Outline each blood parasite and name the species.
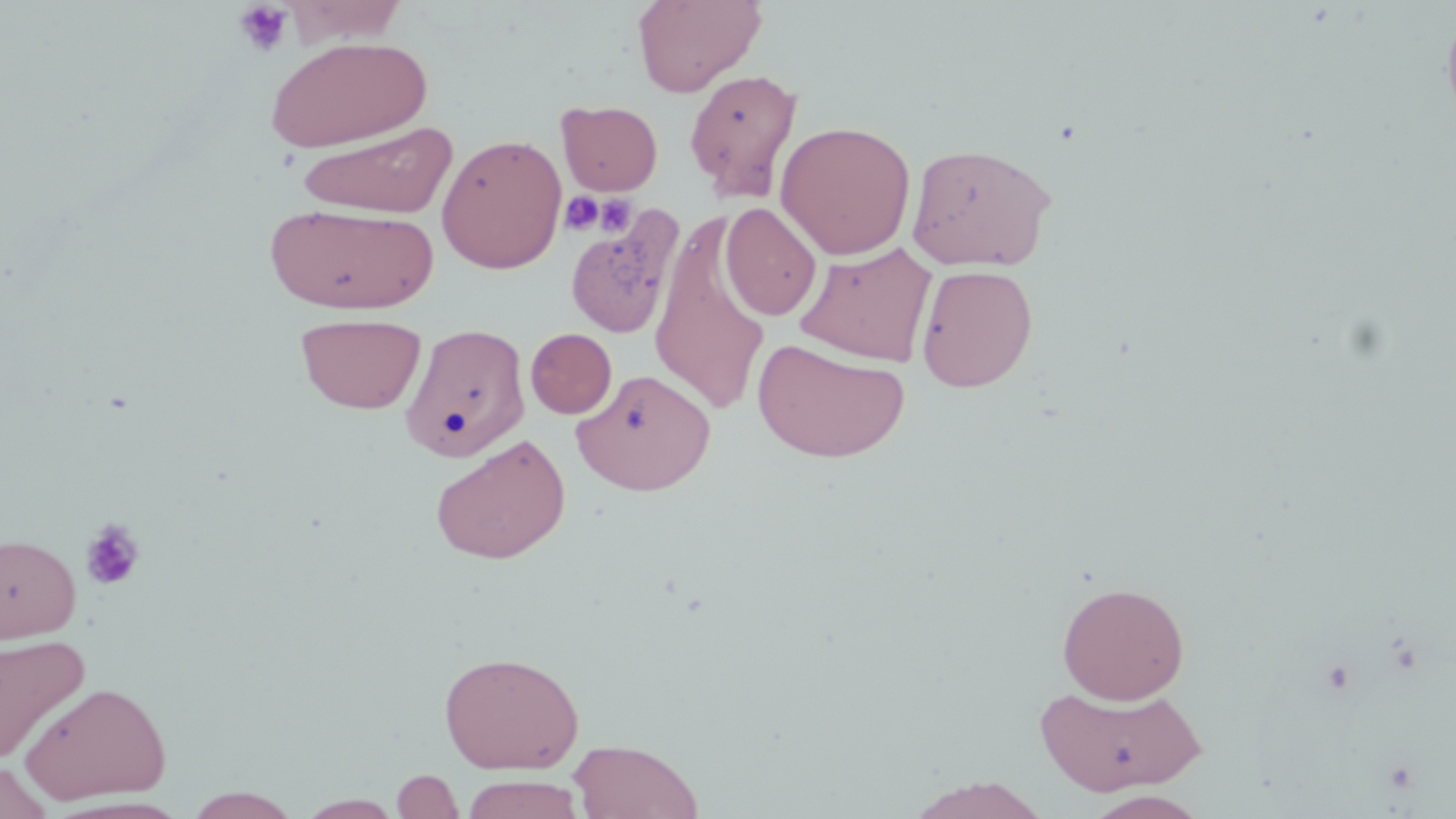

No blood parasites seen.

Summary:
  - Coordinate format: approximate bounding boxes as (x1, y1, x2, y2) in pixels
  - Uninfected red blood cell locations: (631, 0, 767, 97), (1441, 6, 1456, 131), (264, 35, 432, 153), (683, 68, 803, 201), (556, 99, 663, 195), (775, 120, 916, 260), (296, 122, 458, 219), (436, 133, 567, 274), (906, 142, 1057, 271), (265, 201, 438, 315), (720, 202, 822, 321), (564, 208, 683, 341), (649, 214, 773, 416), (794, 241, 937, 366), (915, 264, 1039, 392), (295, 313, 427, 414), (401, 322, 530, 463), (526, 328, 617, 418), (753, 337, 911, 463), (572, 369, 716, 495), (430, 434, 571, 564), (0, 533, 81, 643), (1056, 581, 1190, 704), (0, 633, 90, 764), (438, 650, 585, 774), (19, 681, 172, 805), (1036, 682, 1206, 796), (568, 739, 704, 819), (1, 758, 53, 818), (391, 769, 465, 818), (457, 775, 586, 818), (904, 776, 1052, 819), (184, 787, 302, 818), (1084, 791, 1210, 819), (295, 794, 405, 818)
  - Platelet locations: (233, 1, 294, 58), (561, 192, 604, 235), (594, 194, 637, 236), (80, 518, 146, 591)
  - Slide-level diagnosis: no evidence of blood parasites
  - Field of view: single
  - Preparation: thin blood smear
  - Image size: 1456×819 pixels
  - Modality: optical microscopy
  - Stain: May-Grünwald-Giemsa
  - Magnification: 1000x